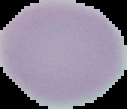

Summary:
  - Result: negative for malaria parasites
  - Image type: segmented cell region on a black background
  - Image size: 127×109 pixels
  - Preparation: thin blood smear